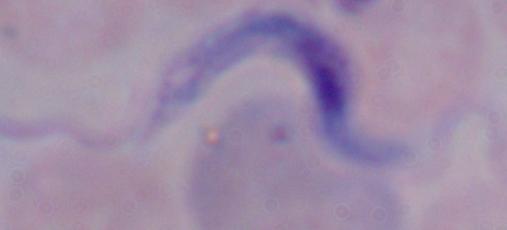

Summary:
  - Modality: micrograph
  - Magnification: 1000x
  - Identification: trypanosome